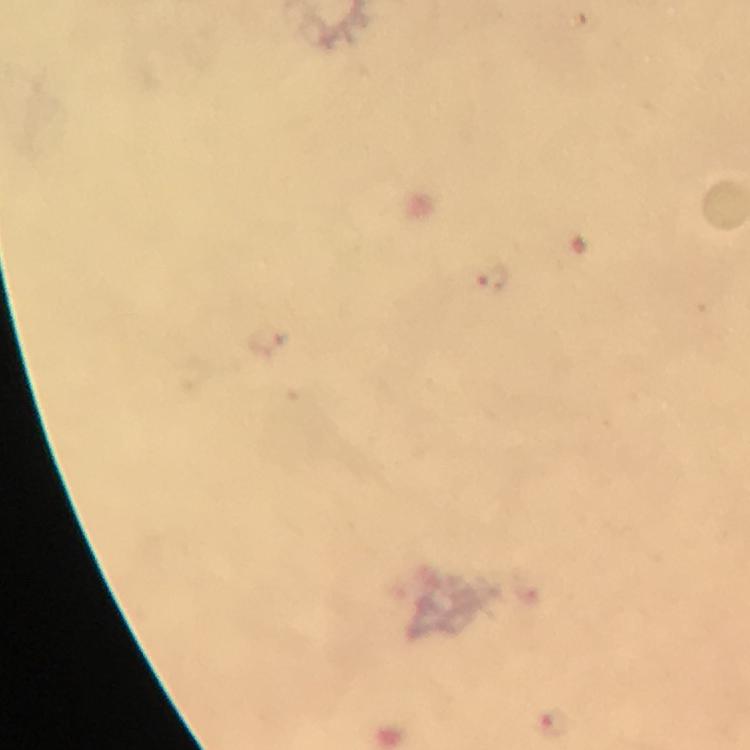

Approximate centers as [x, y] in pixels. Malaria parasite locations: [492, 279], [553, 721]. Photographed with a smartphone mounted on the microscope. Giemsa stain. Thick smear. At 100x magnification. From a diagnostic examination for malaria. Cropped region of a single field of view. Immersion oil applied. Image is 750×750 pixels.